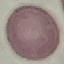
Malaria status: uninfected. Photographed with a smartphone camera at the microscope eyepiece. Giemsa-stained preparation. Thin blood smear. Cell patch, automatically extracted from a larger field of view and resized to 64 × 64 pixels.